Assess this cell for malaria.
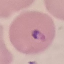
Parasitized.

Summary:
  - Image type: cell patch, automatically extracted from a larger field of view and resized to 64 × 64 pixels
  - Capture: smartphone camera at the microscope eyepiece
  - Stain: Giemsa
  - Preparation: thin smear